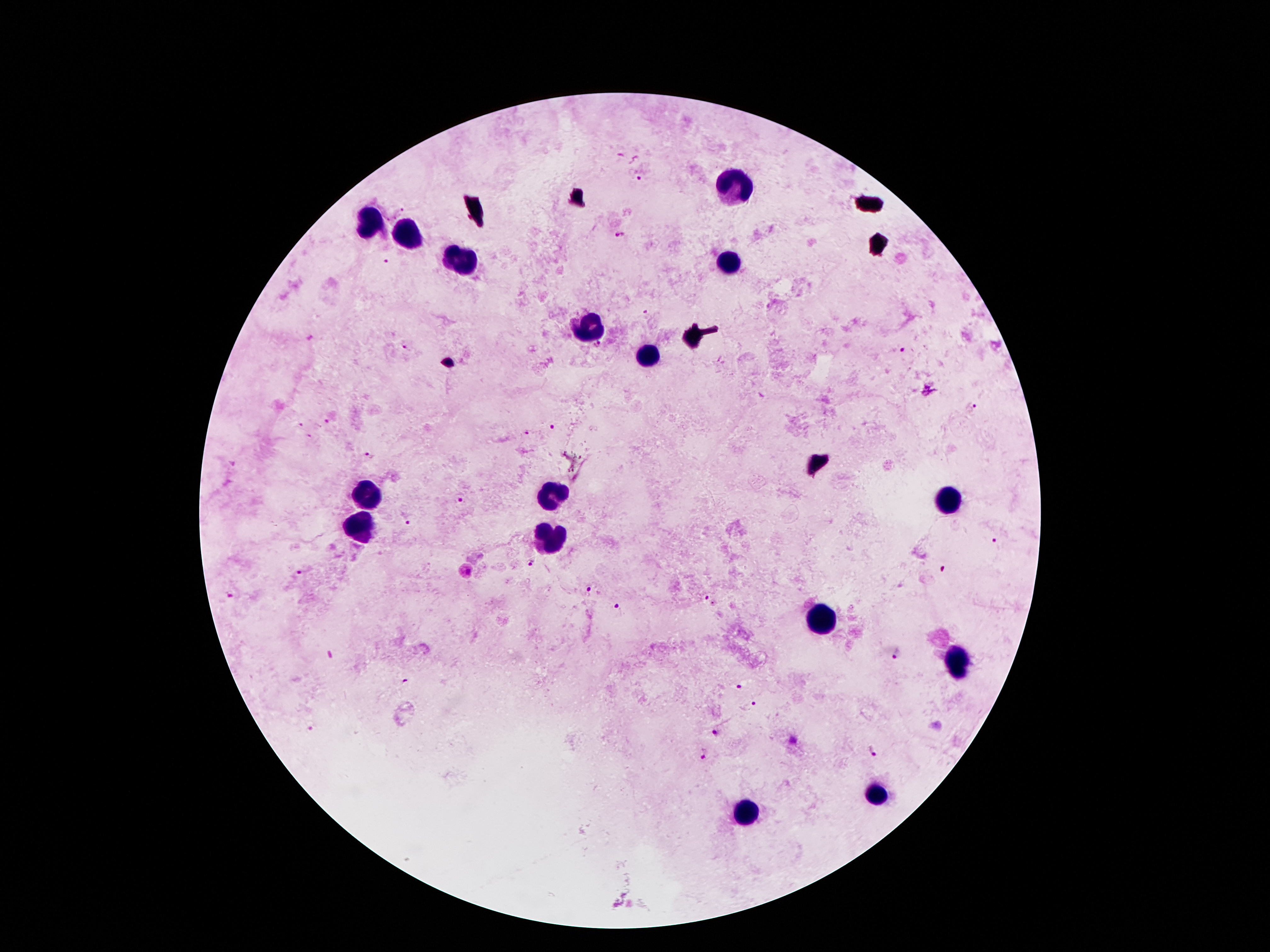
Approximate centers as [x, y] in pixels. Plasmodium parasite locations: [640, 175], [620, 236], [645, 312], [408, 344], [599, 345], [903, 350], [971, 407], [327, 423], [302, 426], [552, 426], [527, 435], [309, 437], [370, 456], [459, 500], [410, 522], [996, 541], [532, 564], [942, 570], [301, 573], [586, 589], [232, 594], [711, 601], [618, 607], [899, 654], [741, 687], [752, 705], [718, 731], [790, 741], [872, 751], [704, 758]. Leukocyte locations: [733, 189], [374, 223], [403, 237], [461, 260], [728, 261], [593, 329], [655, 355], [368, 495], [556, 497], [952, 501], [359, 528], [551, 542], [828, 618], [958, 664], [877, 794], [750, 816]. Smartphone photograph taken through the microscope eyepiece. Giemsa-stained preparation. Patient malaria status: positive for Plasmodium falciparum. Image is 1270×952 pixels. Thick blood film. One field from this slide. 100x magnification.